Report the malaria status of this cell.
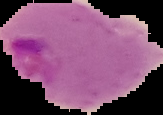
Parasitized.

Summary:
  - Image type: segmented cell region on a black background
  - Preparation: thin blood film
  - Image size: 163×115 pixels